Assess this cell for malaria.
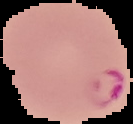

Parasitized.

Image is 133×124 pixels. Cell region segmented out of the field of view; the surrounding area is masked to black. From a thin blood film.